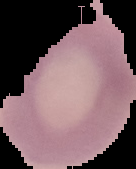

Image is 136×169 pixels. Result: no malaria parasites detected. From a thin blood film. Segmented cell region on a black background.